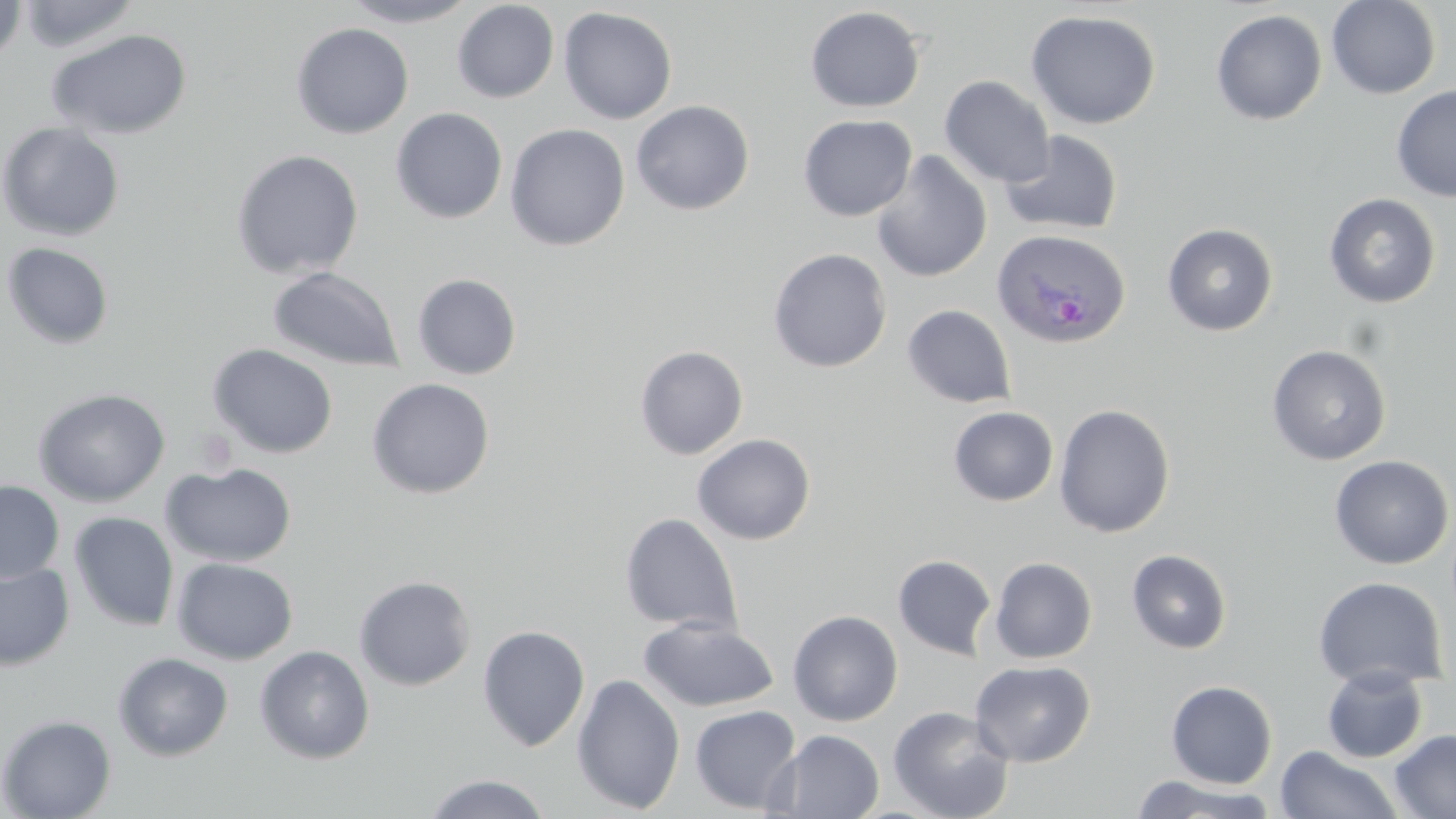

Summary:
  - Coordinate format: approximate bounding boxes as (x1, y1, x2, y2) in pixels
  - Plasmodium ovale-infected red blood cell locations: (991, 228, 1131, 349)
  - Uninfected red blood cell locations: (0, 0, 27, 66), (17, 0, 141, 54), (340, 0, 480, 27), (1326, 0, 1441, 99), (452, 1, 559, 103), (558, 6, 677, 124), (805, 6, 926, 112), (1210, 9, 1328, 125), (1025, 10, 1161, 129), (290, 23, 413, 139), (46, 28, 193, 140), (939, 76, 1055, 188), (1391, 85, 1456, 202), (631, 100, 754, 215), (391, 108, 508, 224), (798, 114, 917, 221), (0, 122, 125, 241), (504, 124, 630, 251), (1000, 130, 1123, 237), (230, 149, 364, 279), (872, 151, 992, 283), (1323, 193, 1441, 308), (1162, 223, 1279, 336), (2, 241, 115, 349), (768, 248, 892, 372), (267, 266, 406, 372), (412, 273, 522, 380), (903, 304, 1017, 408), (207, 344, 339, 459), (1266, 344, 1392, 465), (634, 345, 748, 460), (366, 377, 495, 499), (33, 388, 170, 506), (1053, 404, 1175, 538), (948, 406, 1058, 506), (692, 433, 816, 545), (1329, 455, 1454, 570), (161, 461, 298, 567), (0, 481, 64, 582), (69, 512, 179, 632), (620, 513, 743, 634), (1126, 549, 1232, 654), (892, 554, 997, 659), (172, 557, 298, 665), (989, 557, 1097, 663), (0, 562, 75, 671), (354, 575, 476, 691), (1313, 576, 1448, 691), (787, 610, 903, 726), (638, 616, 779, 713), (477, 624, 590, 751), (255, 645, 375, 764), (112, 652, 234, 762), (970, 660, 1095, 767), (1321, 665, 1429, 763), (572, 673, 685, 814), (1165, 680, 1278, 788), (689, 705, 801, 814), (887, 705, 1015, 819), (0, 714, 117, 819), (1390, 728, 1456, 818), (772, 730, 884, 818), (1274, 745, 1404, 819), (422, 773, 552, 818), (1128, 773, 1279, 818)
  - Slide-level diagnosis: Plasmodium ovale
  - Modality: optical microscopy
  - Preparation: thin blood film
  - Magnification: 1000x
  - Image size: 1456×819 pixels
  - Field of view: one of a larger specimen
  - Stain: May-Grünwald-Giemsa